Name the blood parasite species.
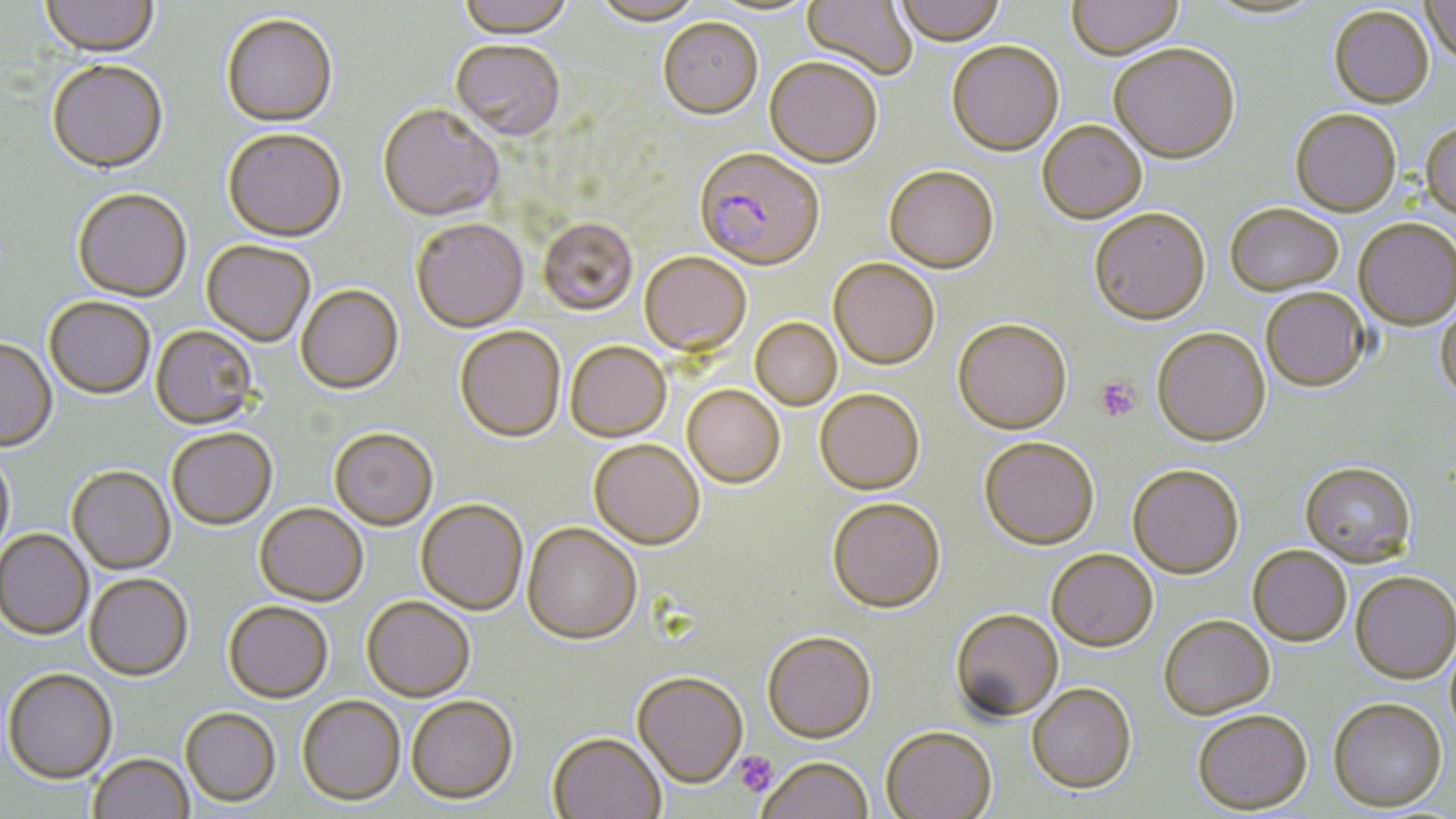

Plasmodium falciparum.

stain = May-Grünwald-Giemsa
Plasmodium falciparum-infected red blood cell locations = approximate bounding boxes as [x1, y1, x2, y2] in pixels: [694, 150, 825, 274]
uninfected red blood cell locations = approximate bounding boxes as [x1, y1, x2, y2] in pixels: [41, 0, 160, 61], [454, 0, 575, 43], [802, 0, 917, 81], [893, 0, 1006, 47], [1420, 0, 1456, 68], [592, 1, 704, 28], [704, 1, 820, 18], [1067, 1, 1184, 63], [1205, 1, 1323, 22], [1329, 7, 1434, 110], [221, 16, 337, 130], [658, 20, 763, 122], [450, 43, 565, 144], [946, 43, 1064, 158], [1109, 47, 1240, 167], [764, 59, 882, 170], [46, 62, 169, 177], [377, 107, 504, 225], [1290, 112, 1401, 219], [1037, 122, 1147, 226], [1420, 123, 1456, 225], [222, 131, 347, 245], [883, 168, 1000, 276], [72, 191, 192, 303], [1225, 206, 1344, 298], [1089, 212, 1211, 329], [538, 220, 638, 318], [411, 221, 529, 334], [1354, 222, 1455, 332], [201, 242, 315, 348], [639, 254, 752, 359], [828, 260, 939, 372], [296, 286, 404, 397], [1261, 291, 1370, 393], [44, 298, 154, 401], [1434, 303, 1456, 405], [750, 319, 842, 411], [953, 322, 1072, 438], [150, 327, 259, 432], [454, 328, 566, 445], [1152, 330, 1271, 449], [0, 340, 58, 453], [565, 343, 672, 444], [682, 387, 785, 491], [814, 392, 925, 498], [329, 430, 437, 532], [167, 431, 277, 532], [979, 440, 1099, 553], [588, 441, 704, 552], [0, 452, 15, 558], [1299, 463, 1417, 570], [67, 467, 176, 576], [1127, 467, 1244, 582], [827, 501, 946, 617], [415, 502, 528, 617], [254, 505, 368, 608], [521, 525, 641, 648], [0, 530, 93, 641], [1247, 548, 1351, 648], [1046, 552, 1158, 655], [1350, 574, 1456, 686], [84, 576, 193, 683], [361, 599, 476, 704], [223, 603, 333, 706], [950, 611, 1063, 724], [1158, 618, 1275, 722], [762, 635, 877, 746], [3, 671, 117, 786], [631, 674, 748, 791], [1026, 685, 1136, 798], [297, 697, 405, 808], [406, 698, 518, 807], [1328, 701, 1447, 814], [180, 710, 281, 809], [1192, 713, 1313, 817], [880, 729, 997, 819], [547, 735, 665, 819], [89, 754, 193, 819], [758, 760, 873, 819]
preparation = thin blood smear
field of view = single
magnification = 1000x
platelet locations = approximate bounding boxes as [x1, y1, x2, y2] in pixels: [1093, 375, 1143, 424], [733, 751, 778, 796]
modality = optical microscopy
image size = 1456×819 pixels